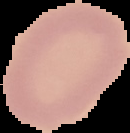
Image is 130×133 pixels. From a thin blood film. The area outside the segmented cell region is set to black. Result: no Plasmodium parasites detected.